Assess this cell for malaria.
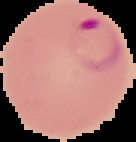

Parasitized.

Image is 136×142 pixels. From a thin blood smear. The area outside the segmented cell region is set to black.